Assess this cell for malaria.
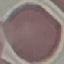
Uninfected.

Cell patch, automatically extracted from a larger field of view and resized to 64 × 64 pixels. Photographed with a smartphone camera at the microscope eyepiece. Giemsa-stained preparation. Thin smear of blood.